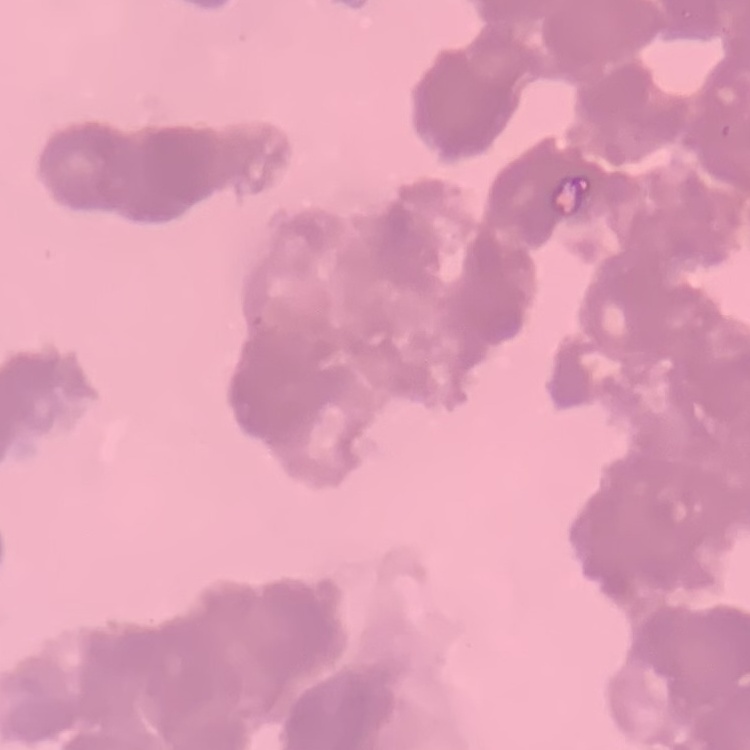 The red blood cells show rouleaux formation. One tile cut from a larger photomicrograph. Stained with either Field's or Giemsa. Thin blood smear.